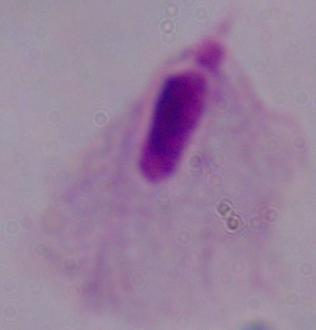
Captured at 1000x magnification. A trichomonad is seen. Micrograph.